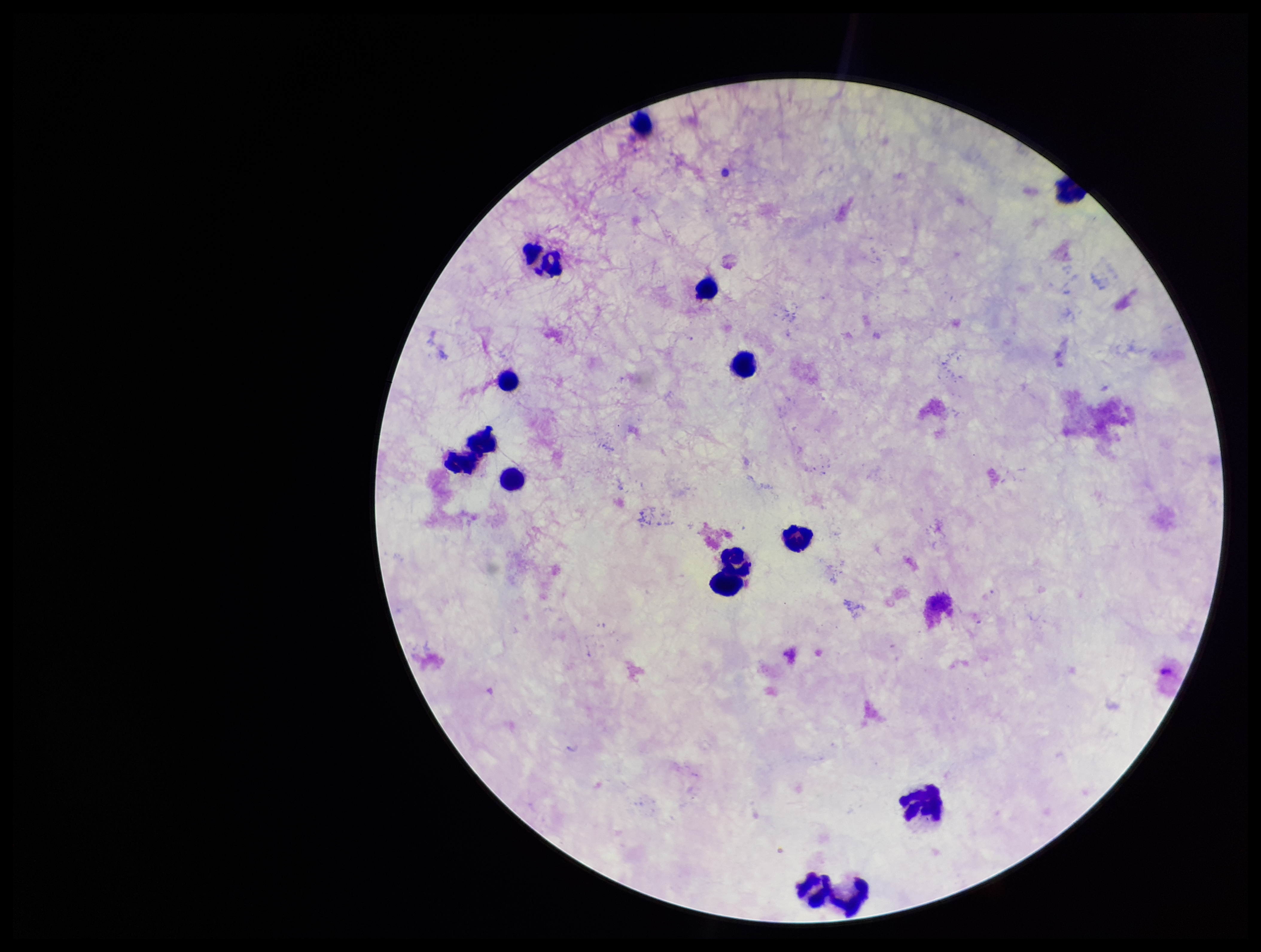

Leukocyte count: 12. Patient malaria status: negative. Preparation: thick blood smear. Stained with Giemsa. Plasmodium parasites: none identified. Image is 1261×952 pixels. Smartphone photograph taken through the eyepiece of a microscope. One field from this slide. Parasite count: 0.